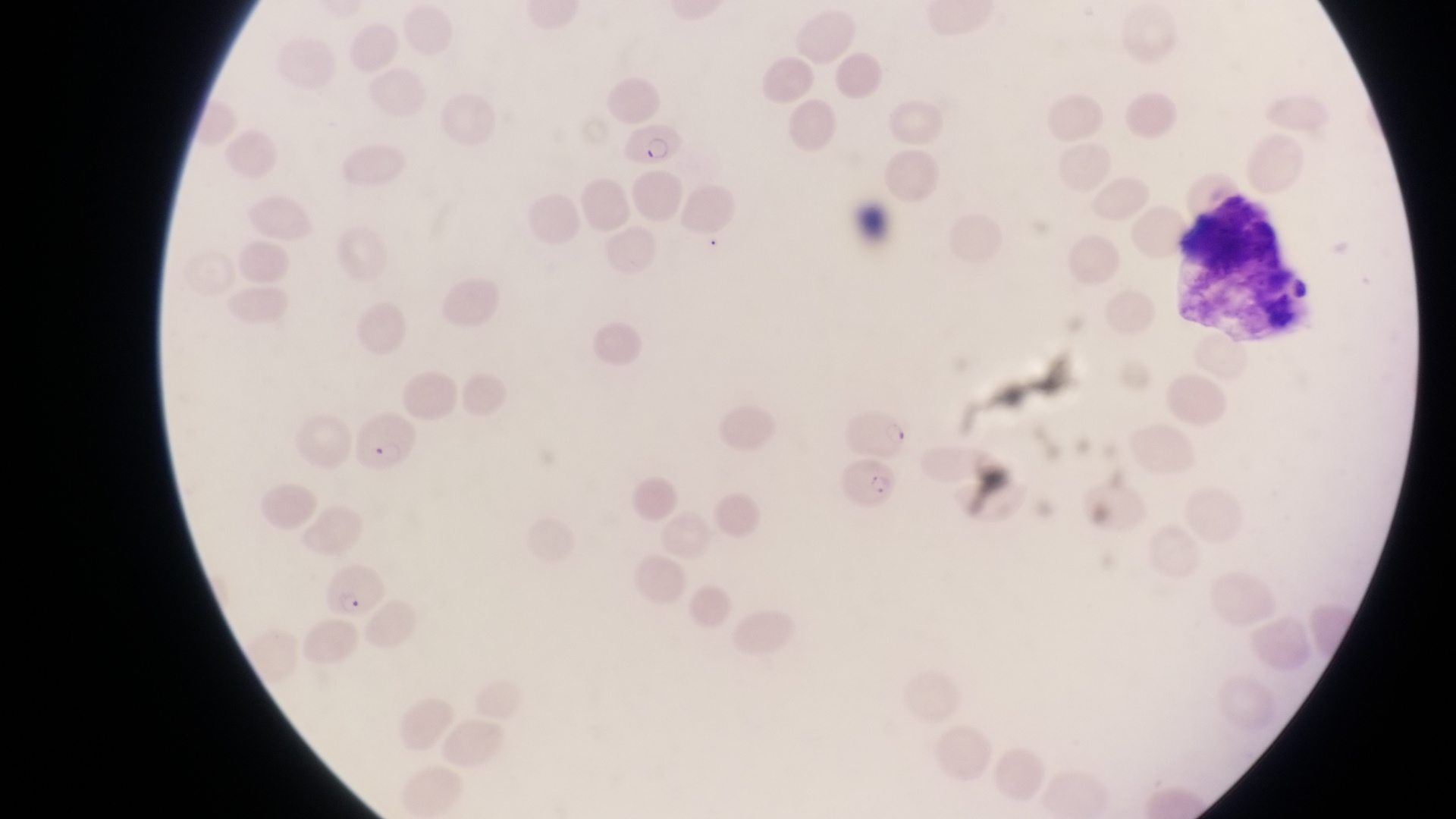

preparation = thin blood smear
field of view = single
image size = 1456×819 pixels
parasitised red blood cell locations = approximate bounding boxes as {left, top, right, bottom} in pixels: {621, 121, 688, 167}, {845, 404, 908, 454}, {353, 416, 422, 476}, {843, 457, 896, 515}, {327, 563, 380, 619}
magnification = 1000x
leukocyte locations = approximate bounding boxes as {left, top, right, bottom} in pixels: {1182, 191, 1311, 333}
capture = smartphone photograph through the eyepiece of an Olympus CX-23 microscope
country = Uganda